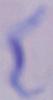 A trypanosome is shown. Micrograph. 1000x magnification.